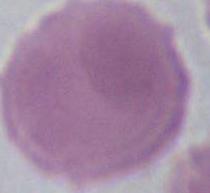
magnification = 1000x
modality = photomicrograph
identification = red blood cell